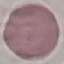

malaria status = uninfected
capture = smartphone through the microscope eyepiece
preparation = thin blood film
stain = Giemsa
image type = cell patch, automatically extracted from a larger field of view and resized to 64 × 64 pixels